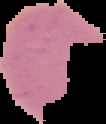
image size = 106×124 pixels
malaria status = uninfected
preparation = thin blood smear
image type = cell region segmented out of the field of view; surrounding area masked to black